Assess this cell for malaria.
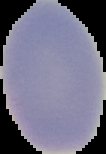

Uninfected.

preparation = thin blood film
image size = 106×154 pixels
image type = segmented cell region with the area outside set to black